Assess this cell for malaria.
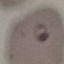

Parasitized.

Acquired by smartphone through the microscope eyepiece. Giemsa-stained preparation. Thin smear of blood. Cell patch, automatically extracted from a larger field of view and resized to 64 × 64 pixels.